Assess this cell for malaria.
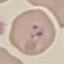

It is parasitized.

stain = Giemsa
preparation = thin blood film
image type = cell patch, automatically extracted from a larger field of view and resized to 64 × 64 pixels
capture = smartphone camera at the microscope eyepiece